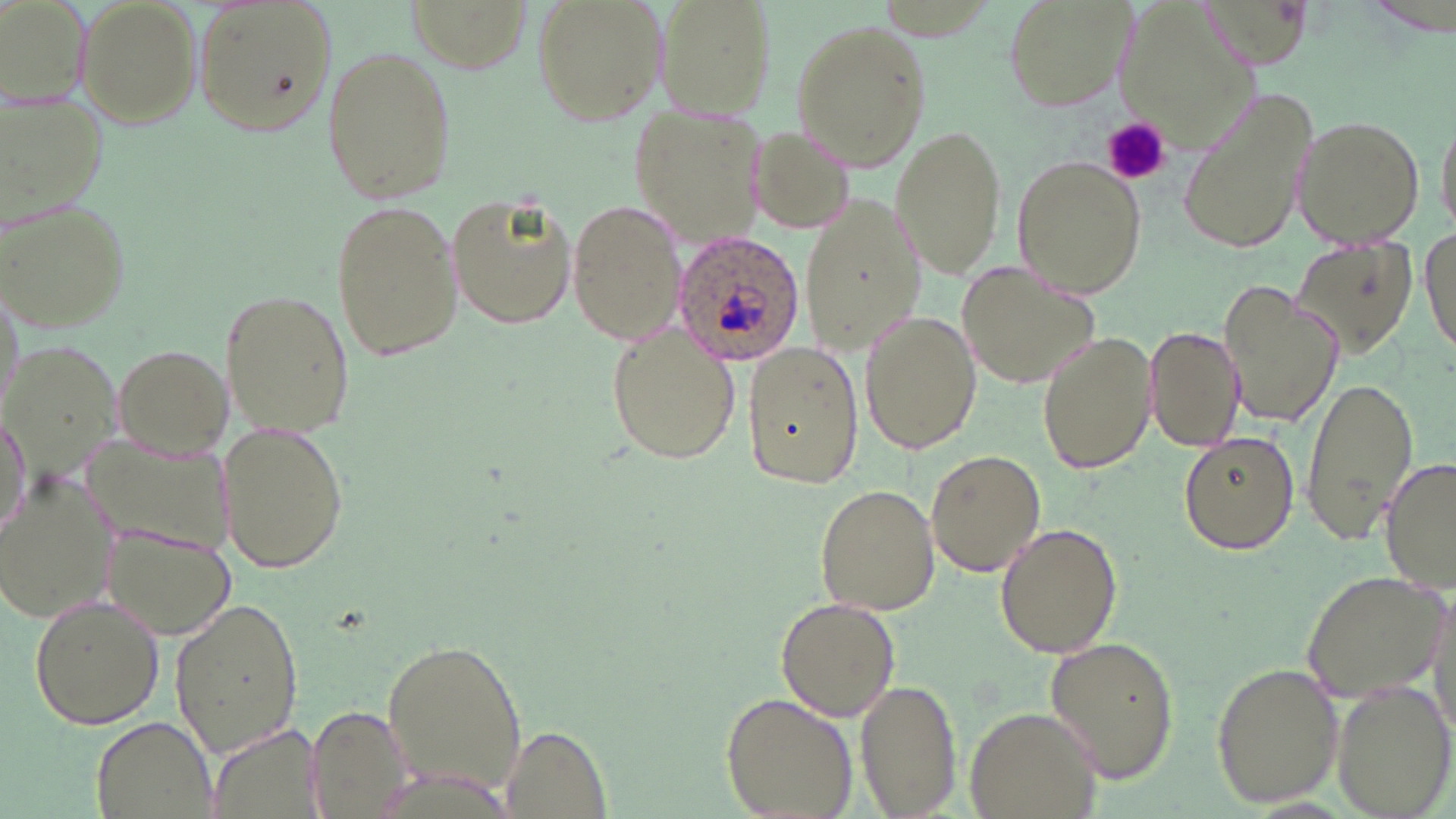

Approximate bounding boxes as named x1/y1/x2/y2 corners in pixels. Platelet locations: (x1=1103, y1=116, x2=1169, y2=186). Plasmodium ovale-infected red blood cell locations: (x1=671, y1=228, x2=808, y2=364). Uninfected red blood cell locations: (x1=75, y1=0, x2=199, y2=124), (x1=192, y1=0, x2=336, y2=136), (x1=530, y1=0, x2=667, y2=127), (x1=658, y1=0, x2=773, y2=117), (x1=1002, y1=0, x2=1135, y2=114), (x1=0, y1=2, x2=91, y2=112), (x1=788, y1=16, x2=933, y2=169), (x1=319, y1=43, x2=457, y2=207), (x1=1177, y1=84, x2=1320, y2=258), (x1=628, y1=105, x2=773, y2=248), (x1=1289, y1=112, x2=1427, y2=249), (x1=891, y1=122, x2=1008, y2=278), (x1=744, y1=123, x2=857, y2=235), (x1=1013, y1=156, x2=1145, y2=297), (x1=447, y1=186, x2=579, y2=336), (x1=802, y1=196, x2=930, y2=353), (x1=329, y1=199, x2=462, y2=364), (x1=566, y1=200, x2=688, y2=347), (x1=2, y1=201, x2=131, y2=335), (x1=1419, y1=230, x2=1454, y2=368), (x1=1289, y1=241, x2=1422, y2=361), (x1=955, y1=259, x2=1100, y2=391), (x1=0, y1=275, x2=25, y2=416), (x1=1219, y1=277, x2=1346, y2=430), (x1=218, y1=288, x2=357, y2=439), (x1=858, y1=312, x2=982, y2=454), (x1=603, y1=322, x2=743, y2=467), (x1=1143, y1=324, x2=1243, y2=454), (x1=1035, y1=329, x2=1158, y2=476), (x1=741, y1=337, x2=864, y2=490), (x1=3, y1=338, x2=128, y2=481), (x1=112, y1=341, x2=233, y2=460), (x1=1300, y1=375, x2=1419, y2=548), (x1=1, y1=408, x2=31, y2=547), (x1=215, y1=419, x2=353, y2=574), (x1=1177, y1=429, x2=1300, y2=556), (x1=924, y1=450, x2=1046, y2=578), (x1=1379, y1=457, x2=1456, y2=594), (x1=0, y1=470, x2=118, y2=622), (x1=814, y1=483, x2=940, y2=616), (x1=101, y1=518, x2=239, y2=640), (x1=993, y1=521, x2=1124, y2=659), (x1=1301, y1=568, x2=1447, y2=704), (x1=28, y1=592, x2=164, y2=730), (x1=167, y1=593, x2=305, y2=760), (x1=776, y1=597, x2=899, y2=721), (x1=378, y1=632, x2=533, y2=804), (x1=1043, y1=637, x2=1180, y2=781), (x1=1211, y1=661, x2=1345, y2=807), (x1=856, y1=675, x2=960, y2=816), (x1=1329, y1=678, x2=1456, y2=819), (x1=722, y1=691, x2=857, y2=819), (x1=964, y1=704, x2=1101, y2=819), (x1=307, y1=705, x2=416, y2=819), (x1=90, y1=713, x2=218, y2=819), (x1=498, y1=727, x2=610, y2=818). Slide-level diagnosis: Plasmodium ovale. 1000x magnification. Thin blood smear. Image is 1456×819 pixels. Single field of view. Optical microscopy. May-Grünwald-Giemsa-stained preparation.